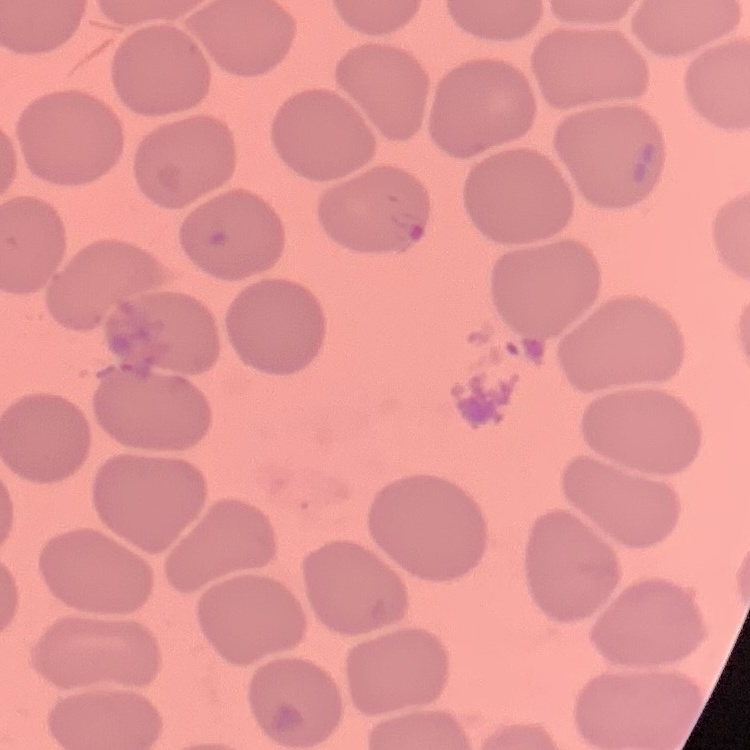 The red blood cells show no rouleaux formation. Thin blood smear. Field's or Giemsa stain. One tile cut from a larger photomicrograph.